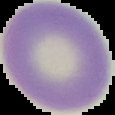

{
  "preparation": "thin blood film",
  "image_size": "115×115 pixels",
  "image_type": "cell region segmented out of the field of view; surrounding area masked to black",
  "malaria_status": "uninfected"
}